Describe the morphology of the red blood cells.
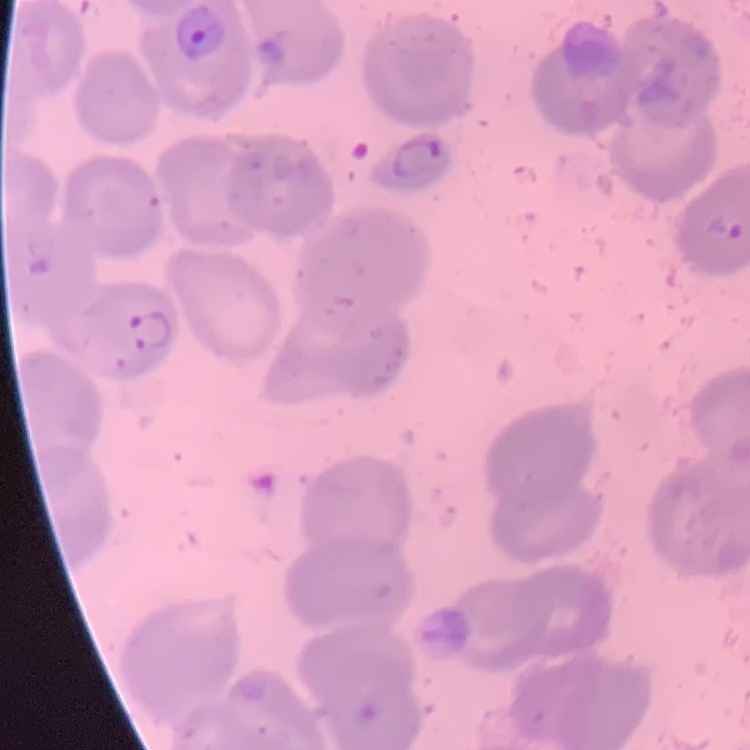

No rouleaux formation.

Summary:
  - Preparation: thin peripheral smear
  - Image type: one tile cut from a larger photomicrograph
  - Stain: Field's or Giemsa